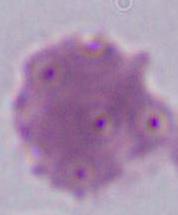 A red blood cell is seen. Captured at 1000x magnification. Photomicrograph.